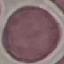

Result: no malaria parasites detected. Giemsa-stained preparation. Automatically extracted cell patch, resized to 64 × 64 pixels. Thin blood film. Acquired by smartphone through the microscope eyepiece.